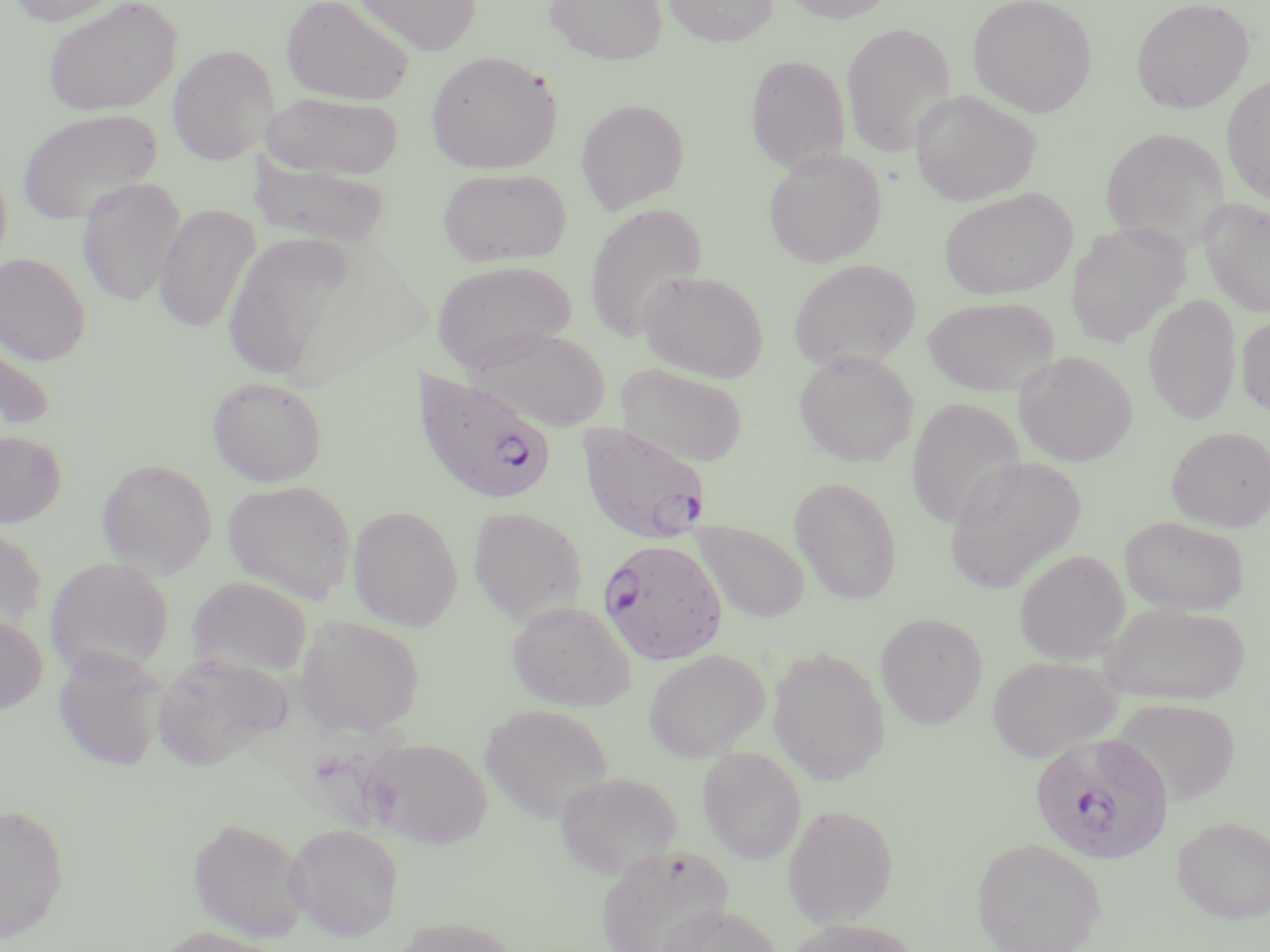
slide-level diagnosis = Plasmodium falciparum
modality = optical microscopy
field of view = one of a larger specimen
magnification = 1000x
uninfected red blood cell locations = approximate bounding boxes as [x1, y1, x2, y2] in pixels: [5, 0, 128, 27], [41, 0, 183, 118], [280, 0, 415, 106], [351, 0, 482, 56], [545, 0, 667, 65], [663, 0, 778, 47], [779, 0, 900, 23], [967, 0, 1098, 118], [1130, 0, 1255, 114], [841, 22, 955, 157], [167, 44, 280, 165], [425, 51, 562, 174], [745, 54, 850, 174], [1221, 73, 1270, 206], [910, 90, 1041, 206], [262, 92, 405, 179], [575, 99, 689, 214], [15, 108, 163, 226], [1099, 128, 1230, 246], [763, 150, 886, 268], [249, 157, 391, 248], [437, 167, 572, 267], [77, 177, 184, 308], [940, 188, 1077, 299], [1199, 197, 1270, 317], [583, 203, 708, 343], [153, 204, 259, 334], [1064, 221, 1193, 349], [224, 232, 359, 381], [0, 252, 91, 365], [789, 259, 922, 371], [431, 260, 576, 372], [638, 270, 770, 383], [1144, 293, 1241, 426], [922, 296, 1061, 396], [1237, 313, 1270, 417], [469, 327, 610, 431], [0, 331, 55, 432], [794, 350, 918, 468], [1014, 350, 1137, 467], [616, 363, 749, 468], [207, 376, 328, 487], [906, 396, 1027, 532], [1167, 426, 1270, 531], [0, 430, 67, 527], [943, 455, 1086, 593], [96, 458, 217, 577], [789, 476, 903, 605], [222, 480, 357, 604], [347, 504, 463, 631], [467, 506, 587, 627], [1119, 516, 1248, 616], [690, 520, 809, 624], [0, 526, 47, 635], [1015, 549, 1130, 665], [45, 557, 174, 679], [187, 576, 312, 681], [507, 600, 636, 711], [1100, 602, 1250, 706], [875, 612, 988, 728], [0, 614, 48, 715], [293, 615, 425, 737], [768, 646, 890, 785], [643, 648, 770, 761], [53, 649, 167, 772], [151, 653, 290, 773], [986, 655, 1122, 763], [1112, 697, 1240, 807], [479, 703, 614, 824], [360, 737, 493, 849], [698, 747, 807, 864], [555, 771, 682, 879], [0, 802, 70, 946], [782, 804, 899, 926], [1172, 816, 1270, 923], [188, 817, 311, 943], [285, 822, 404, 941], [971, 836, 1107, 952], [595, 843, 734, 952], [655, 904, 783, 952], [391, 916, 521, 952], [785, 918, 924, 952], [151, 926, 284, 952]
preparation = thin blood smear
image size = 1270×952 pixels
stain = May-Grünwald-Giemsa
Plasmodium falciparum-infected red blood cell locations = approximate bounding boxes as [x1, y1, x2, y2] in pixels: [410, 368, 557, 507], [575, 423, 712, 545], [600, 548, 736, 663], [1029, 731, 1175, 865]